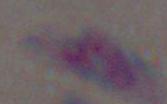
magnification = 1000x
identification = Toxoplasma gondii
modality = micrograph